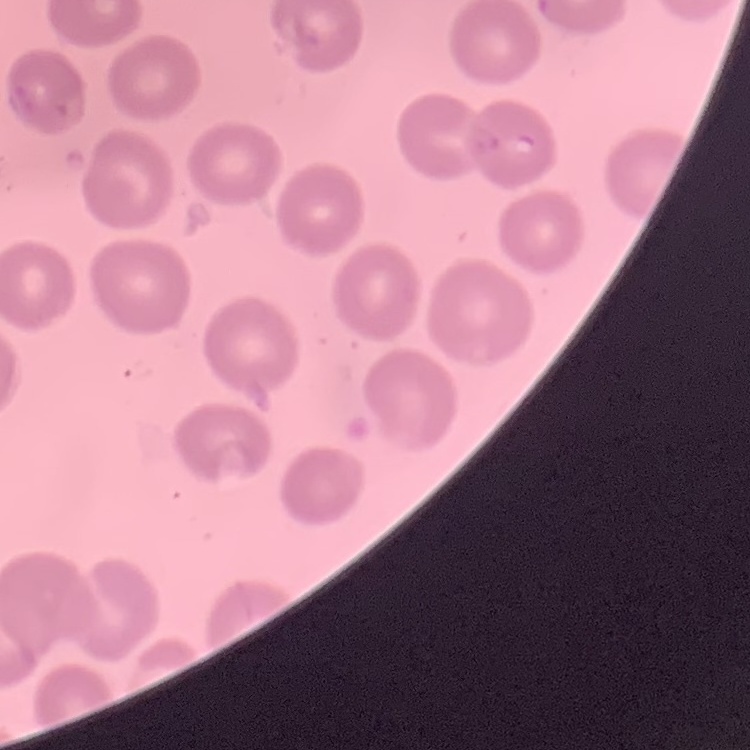
erythrocyte morphology = no rouleaux formation
stain = Field's or Giemsa
preparation = thin blood smear
image type = one tile cut from a larger photomicrograph